Describe the morphology of the erythrocytes.
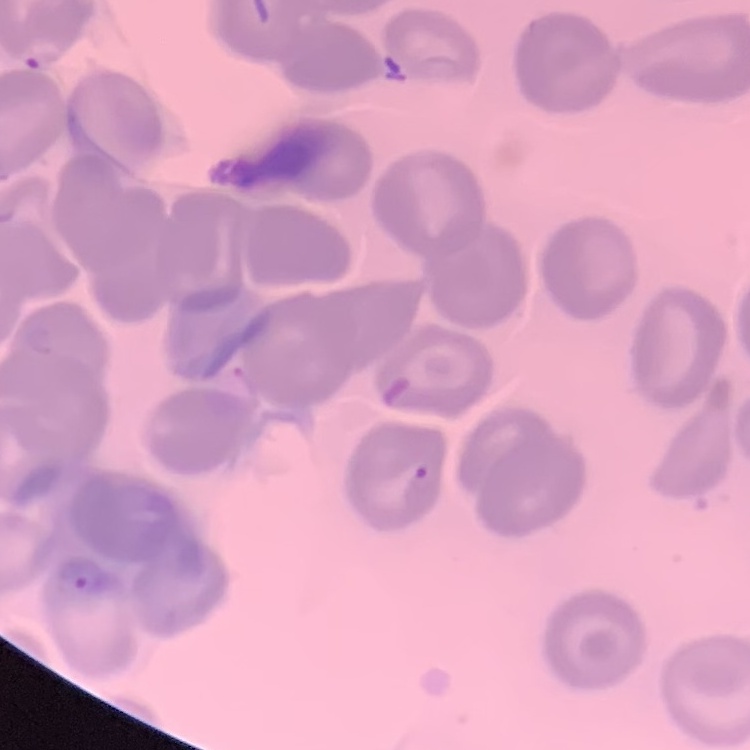
They show no rouleaux formation.

preparation = thin blood film
image type = one tile cut from a larger photomicrograph
stain = Field's or Giemsa